Assess this cell for malaria.
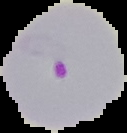
Parasitized.

Image is 127×133 pixels. From a thin blood smear. The area outside the segmented cell region is set to black.